Identify the cell.
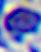

This is a leukocyte.

magnification = 400x
modality = micrograph